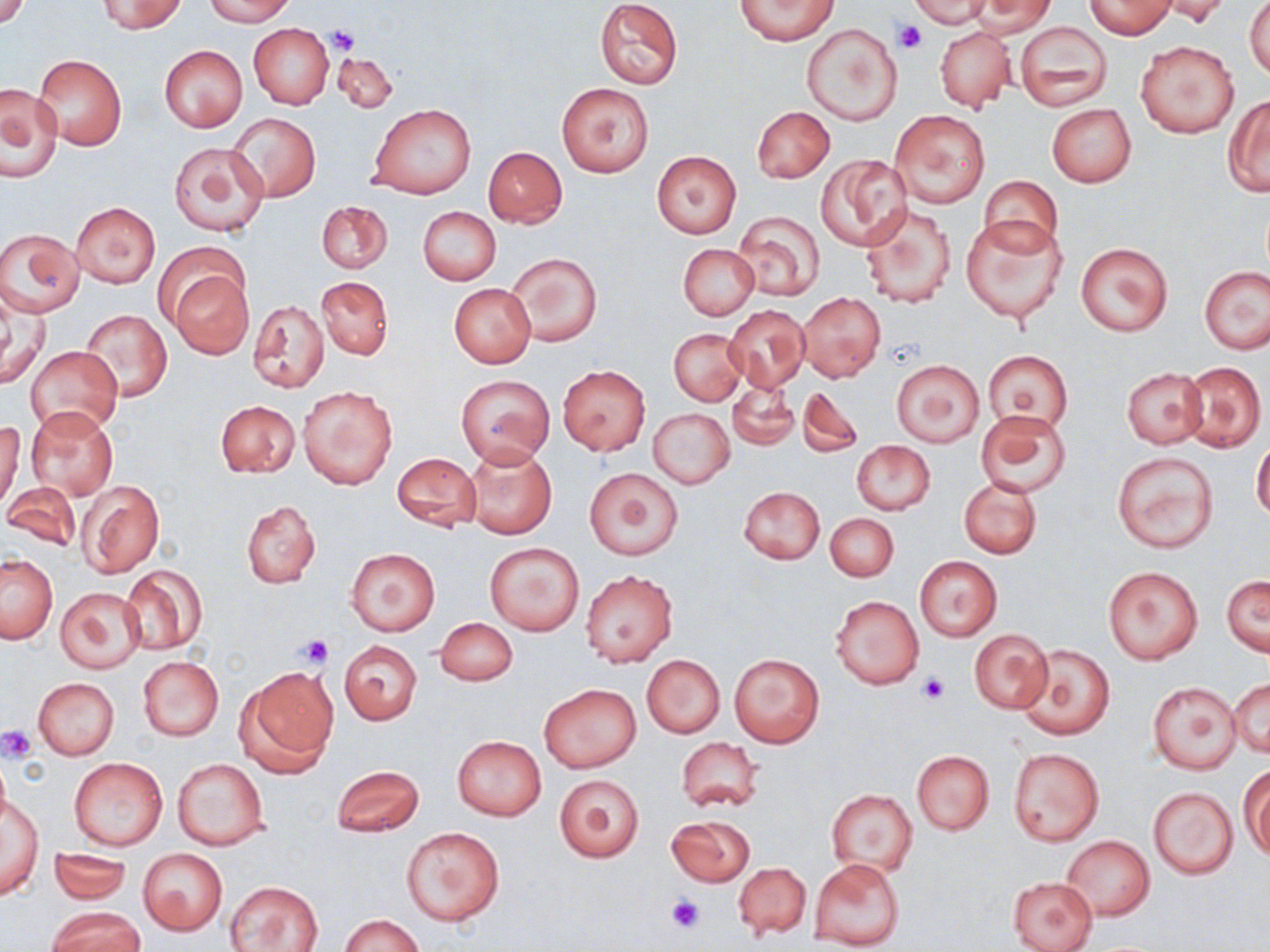
{
  "slide_level_diagnosis": "negative for blood parasites",
  "magnification": "1000x",
  "field_of_view": "one of a larger specimen",
  "uninfected_red_blood_cell_locations": "approximate bounding boxes as named x1/y1/x2/y2 corners in pixels: (x1=97, y1=0, x2=186, y2=34), (x1=205, y1=0, x2=295, y2=25), (x1=595, y1=0, x2=683, y2=89), (x1=735, y1=0, x2=837, y2=44), (x1=910, y1=0, x2=990, y2=28), (x1=1153, y1=0, x2=1233, y2=27), (x1=1244, y1=0, x2=1269, y2=78), (x1=0, y1=1, x2=32, y2=30), (x1=965, y1=1, x2=1056, y2=37), (x1=1085, y1=1, x2=1176, y2=38), (x1=1014, y1=20, x2=1112, y2=110), (x1=802, y1=23, x2=902, y2=125), (x1=248, y1=24, x2=333, y2=109), (x1=935, y1=27, x2=1015, y2=110), (x1=1136, y1=39, x2=1238, y2=138), (x1=159, y1=45, x2=247, y2=132), (x1=332, y1=52, x2=398, y2=113), (x1=32, y1=53, x2=126, y2=151), (x1=557, y1=82, x2=654, y2=178), (x1=0, y1=84, x2=62, y2=183), (x1=1223, y1=96, x2=1270, y2=195), (x1=369, y1=104, x2=475, y2=200), (x1=1047, y1=104, x2=1137, y2=187), (x1=753, y1=106, x2=833, y2=183), (x1=891, y1=111, x2=990, y2=208), (x1=228, y1=113, x2=320, y2=201), (x1=168, y1=142, x2=269, y2=238), (x1=484, y1=147, x2=567, y2=227), (x1=651, y1=150, x2=742, y2=239), (x1=816, y1=155, x2=911, y2=251), (x1=979, y1=176, x2=1062, y2=256), (x1=316, y1=200, x2=392, y2=274), (x1=70, y1=201, x2=160, y2=288), (x1=859, y1=201, x2=956, y2=307), (x1=417, y1=207, x2=501, y2=286), (x1=731, y1=209, x2=825, y2=300), (x1=961, y1=218, x2=1068, y2=324), (x1=1, y1=229, x2=84, y2=317), (x1=1075, y1=242, x2=1172, y2=336), (x1=678, y1=244, x2=758, y2=320), (x1=507, y1=252, x2=601, y2=347), (x1=1200, y1=266, x2=1270, y2=354), (x1=170, y1=268, x2=254, y2=358), (x1=317, y1=277, x2=392, y2=358), (x1=449, y1=283, x2=536, y2=368), (x1=797, y1=292, x2=885, y2=382), (x1=0, y1=297, x2=49, y2=389), (x1=248, y1=300, x2=329, y2=393), (x1=725, y1=305, x2=810, y2=393), (x1=81, y1=308, x2=171, y2=403), (x1=669, y1=328, x2=746, y2=406), (x1=26, y1=344, x2=121, y2=439), (x1=984, y1=351, x2=1074, y2=432), (x1=893, y1=358, x2=985, y2=448), (x1=1179, y1=361, x2=1266, y2=452), (x1=558, y1=365, x2=650, y2=455), (x1=1121, y1=368, x2=1206, y2=448), (x1=457, y1=373, x2=554, y2=467), (x1=727, y1=380, x2=799, y2=450), (x1=298, y1=384, x2=398, y2=491), (x1=798, y1=386, x2=864, y2=458), (x1=216, y1=401, x2=299, y2=478), (x1=24, y1=406, x2=120, y2=501), (x1=648, y1=408, x2=733, y2=489), (x1=976, y1=410, x2=1072, y2=497), (x1=0, y1=421, x2=24, y2=510), (x1=1251, y1=440, x2=1270, y2=521), (x1=852, y1=441, x2=934, y2=515), (x1=463, y1=446, x2=556, y2=539), (x1=1112, y1=451, x2=1218, y2=554), (x1=392, y1=453, x2=481, y2=530), (x1=584, y1=468, x2=683, y2=560), (x1=959, y1=477, x2=1042, y2=559), (x1=3, y1=480, x2=83, y2=550), (x1=77, y1=480, x2=164, y2=578), (x1=739, y1=486, x2=825, y2=564), (x1=242, y1=501, x2=320, y2=588), (x1=825, y1=512, x2=898, y2=581), (x1=484, y1=543, x2=583, y2=635), (x1=345, y1=547, x2=440, y2=636), (x1=0, y1=554, x2=57, y2=642), (x1=913, y1=555, x2=1003, y2=641), (x1=120, y1=565, x2=207, y2=655), (x1=1102, y1=565, x2=1203, y2=664), (x1=580, y1=570, x2=677, y2=667), (x1=1223, y1=576, x2=1269, y2=656), (x1=55, y1=586, x2=146, y2=672), (x1=830, y1=594, x2=924, y2=690), (x1=435, y1=617, x2=518, y2=687), (x1=969, y1=630, x2=1053, y2=713), (x1=339, y1=641, x2=422, y2=724), (x1=1016, y1=643, x2=1114, y2=740), (x1=730, y1=653, x2=824, y2=748), (x1=642, y1=655, x2=725, y2=737), (x1=138, y1=656, x2=224, y2=740), (x1=237, y1=667, x2=338, y2=776), (x1=33, y1=676, x2=119, y2=760), (x1=1229, y1=679, x2=1270, y2=758), (x1=1148, y1=682, x2=1241, y2=773), (x1=540, y1=684, x2=641, y2=773), (x1=452, y1=735, x2=548, y2=821), (x1=676, y1=737, x2=763, y2=812), (x1=1008, y1=746, x2=1104, y2=845), (x1=911, y1=750, x2=994, y2=835), (x1=69, y1=757, x2=169, y2=851), (x1=173, y1=758, x2=269, y2=852), (x1=331, y1=764, x2=425, y2=837), (x1=1241, y1=767, x2=1269, y2=862), (x1=555, y1=773, x2=644, y2=862), (x1=1148, y1=786, x2=1238, y2=880), (x1=826, y1=788, x2=917, y2=875), (x1=2, y1=796, x2=43, y2=900), (x1=668, y1=816, x2=754, y2=886), (x1=400, y1=827, x2=504, y2=926), (x1=1061, y1=836, x2=1154, y2=920), (x1=48, y1=846, x2=133, y2=905), (x1=137, y1=848, x2=228, y2=935), (x1=810, y1=859, x2=905, y2=949), (x1=733, y1=862, x2=812, y2=938), (x1=1008, y1=876, x2=1098, y2=951), (x1=227, y1=881, x2=323, y2=951), (x1=49, y1=907, x2=144, y2=952), (x1=341, y1=914, x2=422, y2=952)",
  "platelet_locations": "approximate bounding boxes as named x1/y1/x2/y2 corners in pixels: (x1=893, y1=18, x2=925, y2=54), (x1=327, y1=27, x2=360, y2=55), (x1=295, y1=634, x2=335, y2=668), (x1=916, y1=671, x2=951, y2=703), (x1=0, y1=725, x2=36, y2=762), (x1=667, y1=895, x2=703, y2=933)",
  "stain": "May-Grünwald-Giemsa",
  "modality": "optical microscopy",
  "image_size": "1270×952 pixels",
  "preparation": "thin blood film"
}